Identify the parasite.
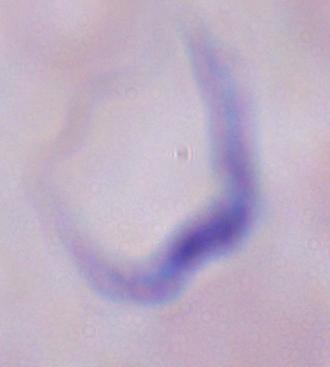
This is a trypanosome.

1000x magnification. Photomicrograph.